Give the extent of all uninfected red blood cells.
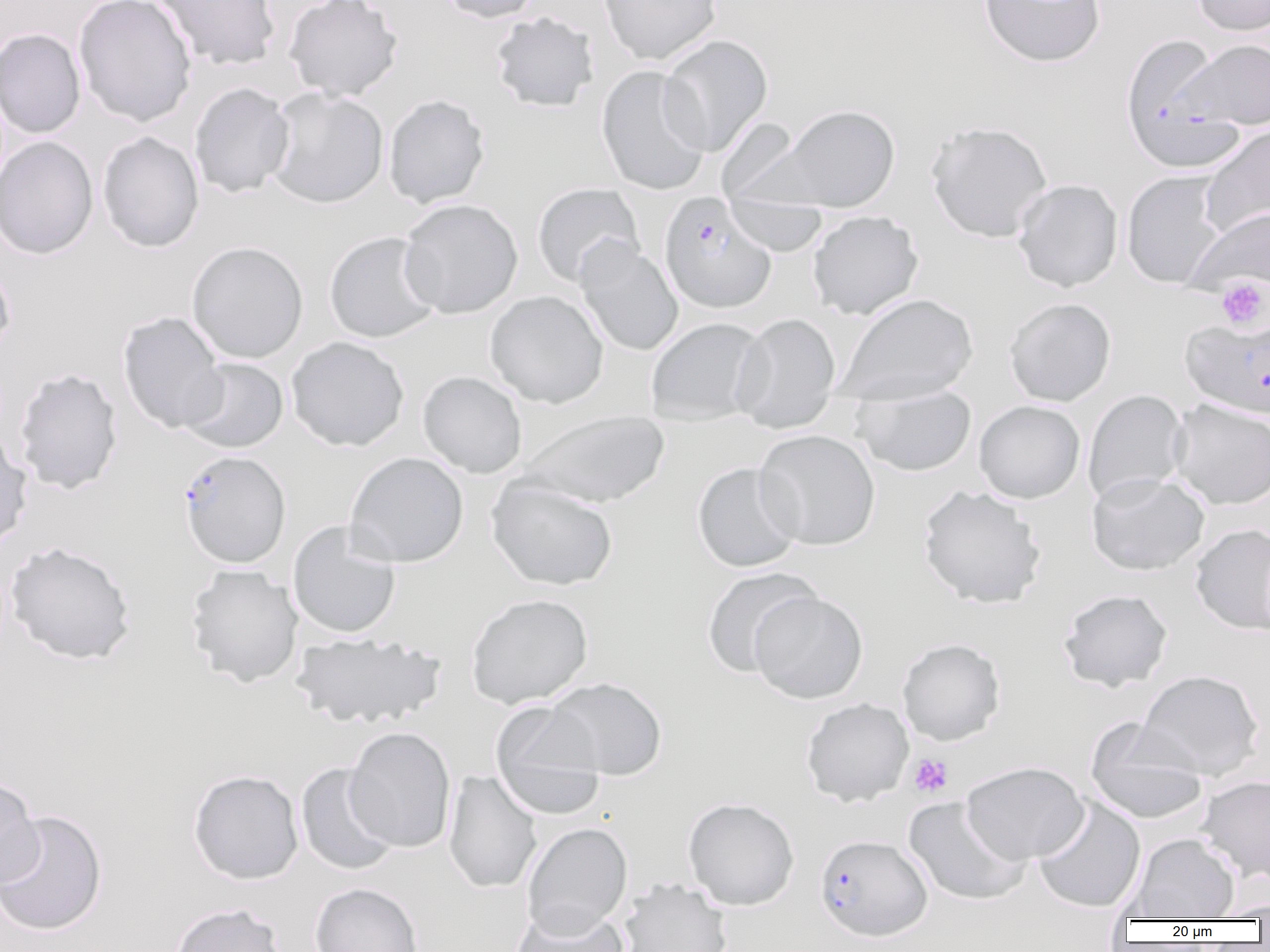

Approximate bounding boxes as (x1,y1)-(x2,y2) corner pairs in pixels.
Uninfected red blood cells: (73,0)-(197,126), (149,0)-(281,71), (283,0)-(403,101), (436,0)-(543,23), (598,0)-(722,64), (979,0)-(1106,67), (1192,0)-(1270,36), (490,11)-(599,113), (0,28)-(86,138), (659,34)-(773,157), (1180,37)-(1270,129), (595,65)-(712,196), (188,82)-(295,198), (264,87)-(389,209), (383,94)-(490,208), (776,104)-(900,212), (715,116)-(814,211), (925,119)-(1053,242), (1199,125)-(1270,239), (97,131)-(204,252), (0,136)-(98,259), (1121,170)-(1228,288), (1012,179)-(1123,292), (531,182)-(644,288), (723,193)-(829,256), (399,199)-(523,318), (1183,207)-(1270,298), (807,210)-(924,320), (323,230)-(442,343), (575,239)-(683,357), (186,241)-(308,364), (0,258)-(16,361), (484,290)-(609,408), (836,293)-(979,405), (1004,297)-(1117,406), (117,311)-(228,433), (732,312)-(841,433), (645,317)-(769,425), (286,336)-(409,451), (180,357)-(289,453), (12,367)-(123,495), (417,371)-(528,478), (852,385)-(977,476), (1083,389)-(1189,504), (973,400)-(1086,504), (1169,400)-(1270,510), (519,410)-(670,508), (0,428)-(33,550), (755,429)-(880,551), (345,451)-(469,568), (692,462)-(803,572), (1087,472)-(1209,576), (486,476)-(619,591), (917,485)-(1047,609), (287,521)-(402,639), (1190,523)-(1270,635), (3,540)-(136,665), (185,564)-(303,688), (701,567)-(821,677), (1058,588)-(1173,692), (748,591)-(869,703), (465,593)-(593,708), (290,633)-(446,729), (897,637)-(1006,746), (1136,669)-(1264,779), (545,677)-(667,781), (801,697)-(913,807), (490,701)-(606,818), (1085,717)-(1209,825), (344,726)-(456,853), (961,761)-(1089,864), (295,763)-(400,876), (188,769)-(304,884), (444,770)-(543,894), (1196,775)-(1270,884), (0,776)-(43,889), (1032,796)-(1146,913), (683,797)-(799,911), (902,797)-(1031,906), (0,809)-(107,936), (522,822)-(633,937), (1128,833)-(1240,920), (618,877)-(732,952), (309,882)-(423,952), (1209,898)-(1270,920), (169,902)-(289,952), (512,905)-(629,951).

Summary:
  - Platelet locations: (1215,276)-(1269,331), (907,753)-(954,798)
  - Plasmodium falciparum-infected red blood cell locations: (1119,32)-(1241,173), (660,192)-(777,314), (1180,315)-(1270,419), (178,450)-(291,568), (814,833)-(932,941)
  - Slide-level diagnosis: Plasmodium falciparum
  - Image size: 1270×952 pixels
  - Preparation: thin blood film
  - Modality: light microscopy
  - Magnification: 1000x
  - Field of view: single